Point out each malaria parasite.
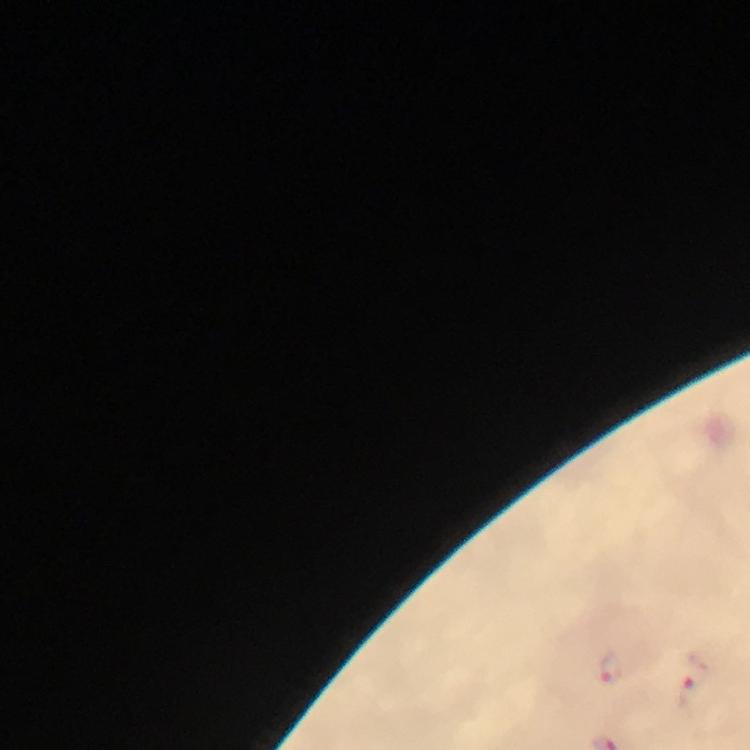

Approximate object centers, in pixels from the top-left corner.
Malaria parasites: (x=609, y=667), (x=692, y=681).

Summary:
  - Magnification: 100x
  - Cropped from: one field of view
  - Image size: 750×750 pixels
  - Stain: Giemsa
  - Immersion oil: applied
  - Preparation: thick smear
  - Context: from a diagnostic examination for malaria
  - Capture: smartphone mounted on the microscope